Name the cell type shown.
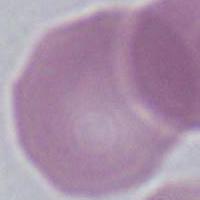
This is an erythrocyte.

Summary:
  - Modality: photomicrograph
  - Magnification: 1000x